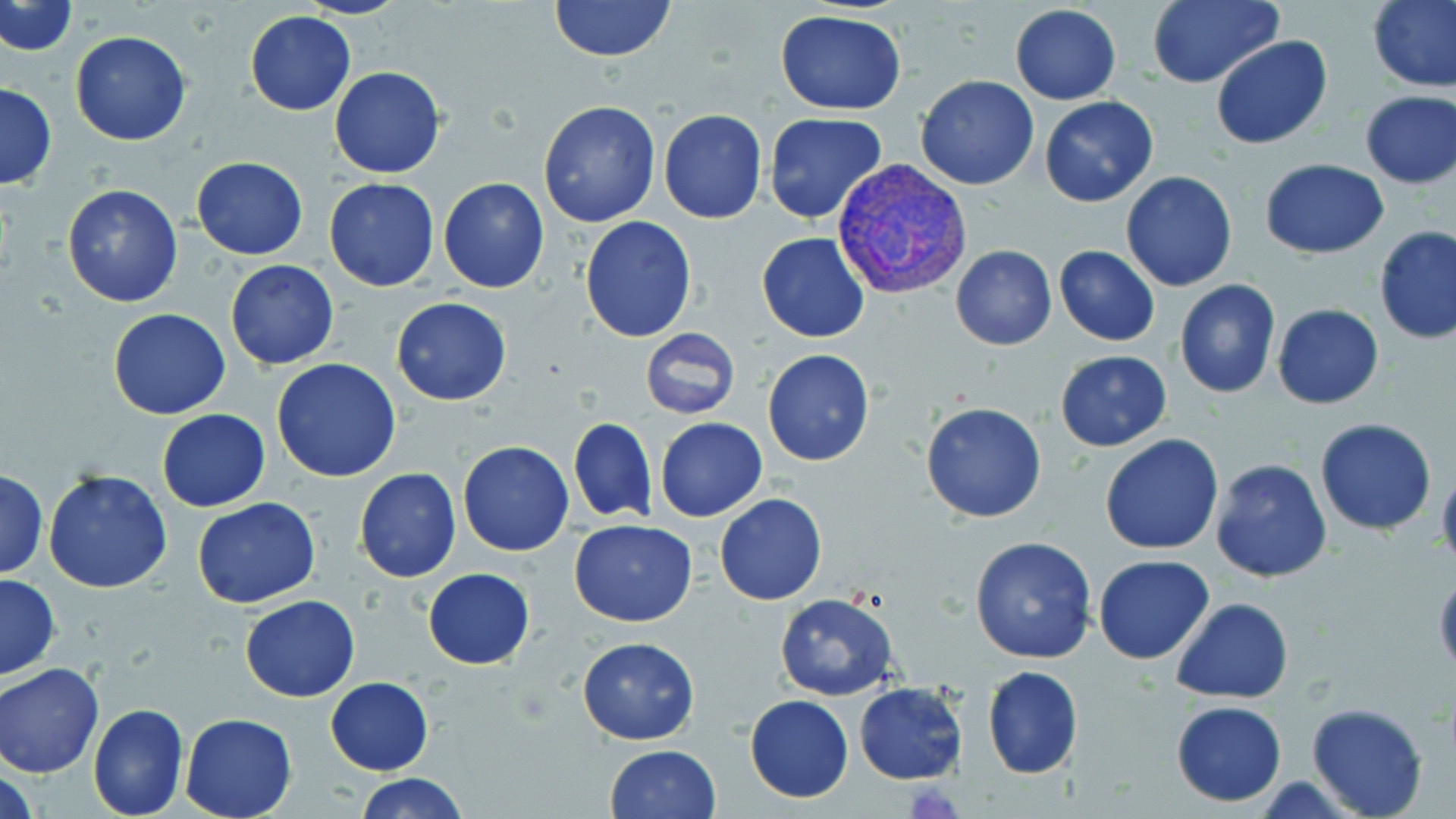

slide_level_diagnosis: Plasmodium vivax
uninfected_red_blood_cell_locations: 'approximate bounding boxes as named x1/y1/x2/y2 corners in pixels: (x1=297, y1=0, x2=408, y2=20), (x1=549, y1=0, x2=675, y2=63), (x1=1369, y1=0, x2=1456, y2=92), (x1=1, y1=1, x2=76, y2=56), (x1=1145, y1=1, x2=1281, y2=89), (x1=1010, y1=3, x2=1121, y2=104), (x1=774, y1=9, x2=908, y2=114), (x1=244, y1=10, x2=355, y2=115), (x1=70, y1=29, x2=193, y2=146), (x1=1210, y1=36, x2=1333, y2=151), (x1=329, y1=66, x2=445, y2=179), (x1=915, y1=75, x2=1040, y2=190), (x1=0, y1=82, x2=57, y2=192), (x1=1359, y1=89, x2=1455, y2=189), (x1=1040, y1=96, x2=1159, y2=206), (x1=537, y1=100, x2=662, y2=227), (x1=657, y1=109, x2=768, y2=224), (x1=764, y1=113, x2=888, y2=223), (x1=191, y1=156, x2=309, y2=259), (x1=1260, y1=159, x2=1389, y2=257), (x1=1119, y1=171, x2=1239, y2=293), (x1=438, y1=176, x2=550, y2=293), (x1=323, y1=177, x2=441, y2=291), (x1=60, y1=183, x2=184, y2=307), (x1=580, y1=215, x2=697, y2=343), (x1=1374, y1=226, x2=1456, y2=345), (x1=757, y1=232, x2=870, y2=343), (x1=950, y1=245, x2=1057, y2=351), (x1=1054, y1=246, x2=1160, y2=345), (x1=225, y1=259, x2=341, y2=370), (x1=1174, y1=280, x2=1282, y2=400), (x1=391, y1=298, x2=512, y2=405), (x1=1273, y1=303, x2=1384, y2=409), (x1=107, y1=308, x2=231, y2=420), (x1=639, y1=328, x2=741, y2=419), (x1=762, y1=350, x2=875, y2=466), (x1=1055, y1=350, x2=1173, y2=453), (x1=271, y1=359, x2=403, y2=482), (x1=921, y1=401, x2=1048, y2=523), (x1=156, y1=410, x2=271, y2=511), (x1=567, y1=416, x2=657, y2=525), (x1=655, y1=417, x2=767, y2=521), (x1=1314, y1=418, x2=1436, y2=535), (x1=1099, y1=434, x2=1223, y2=555), (x1=458, y1=441, x2=574, y2=556), (x1=1208, y1=458, x2=1333, y2=584), (x1=1436, y1=462, x2=1456, y2=577), (x1=353, y1=467, x2=462, y2=583), (x1=0, y1=469, x2=48, y2=580), (x1=42, y1=470, x2=173, y2=593), (x1=715, y1=493, x2=827, y2=605), (x1=191, y1=496, x2=320, y2=609), (x1=569, y1=520, x2=697, y2=627), (x1=969, y1=534, x2=1097, y2=666), (x1=1094, y1=554, x2=1213, y2=665), (x1=1433, y1=567, x2=1456, y2=679), (x1=423, y1=568, x2=535, y2=669), (x1=0, y1=571, x2=61, y2=681), (x1=774, y1=594, x2=898, y2=701), (x1=241, y1=595, x2=360, y2=701), (x1=1171, y1=598, x2=1294, y2=703), (x1=577, y1=637, x2=701, y2=745), (x1=0, y1=662, x2=105, y2=778), (x1=982, y1=667, x2=1084, y2=779), (x1=326, y1=677, x2=433, y2=776), (x1=853, y1=682, x2=969, y2=784), (x1=745, y1=695, x2=852, y2=803), (x1=1170, y1=700, x2=1287, y2=806), (x1=88, y1=702, x2=189, y2=819), (x1=1306, y1=704, x2=1430, y2=819), (x1=180, y1=713, x2=298, y2=819), (x1=604, y1=744, x2=723, y2=819), (x1=357, y1=772, x2=469, y2=819)'
stain: May-Grünwald-Giemsa
preparation: thin blood film
field_of_view: one of a larger specimen
plasmodium_vivax_infected_red_blood_cell_locations: 'approximate bounding boxes as named x1/y1/x2/y2 corners in pixels: (x1=832, y1=158, x2=973, y2=299)'
modality: light microscopy
magnification: 1000x
image_size: 1456×819 pixels